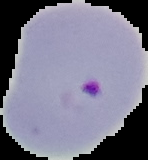 Image is 148×160 pixels. Malaria status: parasitized. Segmented cell region on a black background. From a thin blood smear.